Report the malaria status of this cell.
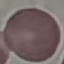
Uninfected.

Summary:
  - Image type: cell patch, automatically extracted from a larger field of view and resized to 64 × 64 pixels
  - Stain: Giemsa
  - Preparation: thin smear
  - Capture: smartphone camera at the microscope eyepiece